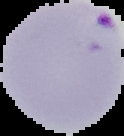
Malaria status: parasitized. From a thin blood smear. The area outside the segmented cell region is set to black. Image is 124×136 pixels.